Assess this cell for malaria.
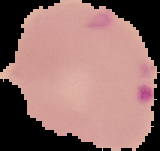

Parasitized.

Segmented cell region on a black background. From a thin blood smear. Image is 160×151 pixels.